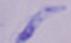 Captured at 1000x magnification. A trypanosome is shown. Micrograph.